Assess this cell for malaria.
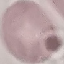
It is uninfected.

Cell patch, automatically extracted from a larger field of view and resized to 64 × 64 pixels. Thin blood film. Giemsa-stained preparation. Acquired by smartphone through the microscope eyepiece.